Classify this cell by malaria status.
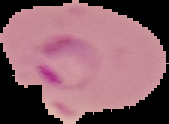
It is parasitized.

The area outside the segmented cell region is set to black. Image is 169×124 pixels. From a thin blood smear.